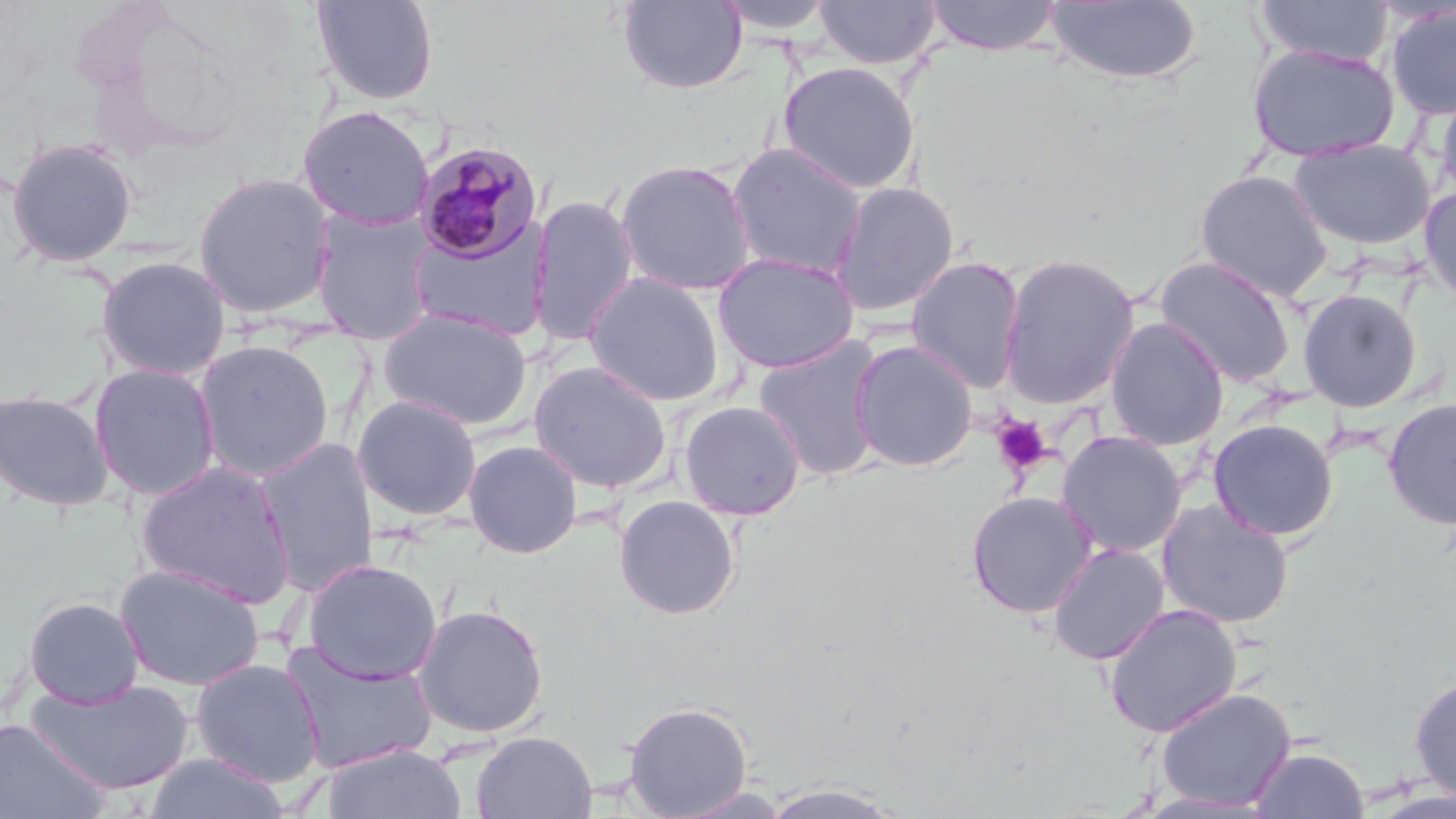
Approximate bounding boxes as named x1/y1/x2/y2 corners in pixels. Uninfected red blood cell locations: (x1=311, y1=0, x2=440, y2=105), (x1=712, y1=0, x2=839, y2=35), (x1=923, y1=0, x2=1065, y2=56), (x1=1253, y1=0, x2=1395, y2=67), (x1=617, y1=1, x2=747, y2=94), (x1=813, y1=1, x2=942, y2=69), (x1=1043, y1=1, x2=1202, y2=84), (x1=1385, y1=5, x2=1456, y2=120), (x1=1246, y1=43, x2=1400, y2=164), (x1=778, y1=61, x2=920, y2=194), (x1=1435, y1=81, x2=1456, y2=205), (x1=297, y1=105, x2=436, y2=230), (x1=4, y1=136, x2=139, y2=268), (x1=1289, y1=138, x2=1436, y2=251), (x1=726, y1=142, x2=868, y2=280), (x1=615, y1=159, x2=758, y2=296), (x1=1194, y1=169, x2=1334, y2=301), (x1=192, y1=171, x2=337, y2=319), (x1=829, y1=180, x2=960, y2=317), (x1=1419, y1=185, x2=1456, y2=305), (x1=528, y1=195, x2=639, y2=347), (x1=308, y1=207, x2=438, y2=344), (x1=404, y1=224, x2=552, y2=343), (x1=712, y1=251, x2=860, y2=374), (x1=997, y1=253, x2=1141, y2=410), (x1=95, y1=255, x2=232, y2=381), (x1=905, y1=255, x2=1026, y2=393), (x1=1155, y1=255, x2=1298, y2=388), (x1=582, y1=272, x2=727, y2=407), (x1=1296, y1=288, x2=1424, y2=413), (x1=378, y1=307, x2=533, y2=429), (x1=1105, y1=317, x2=1229, y2=451), (x1=751, y1=335, x2=887, y2=481), (x1=194, y1=339, x2=334, y2=481), (x1=849, y1=340, x2=979, y2=472), (x1=528, y1=360, x2=673, y2=493), (x1=88, y1=362, x2=222, y2=500), (x1=0, y1=388, x2=115, y2=511), (x1=352, y1=394, x2=483, y2=522), (x1=1383, y1=397, x2=1456, y2=530), (x1=678, y1=399, x2=806, y2=520), (x1=1207, y1=418, x2=1339, y2=541), (x1=1056, y1=430, x2=1188, y2=557), (x1=254, y1=439, x2=380, y2=595), (x1=463, y1=439, x2=583, y2=558), (x1=136, y1=459, x2=296, y2=607), (x1=966, y1=490, x2=1098, y2=618), (x1=613, y1=495, x2=741, y2=620), (x1=1155, y1=499, x2=1295, y2=629), (x1=1046, y1=541, x2=1170, y2=665), (x1=301, y1=558, x2=443, y2=685), (x1=113, y1=563, x2=266, y2=691), (x1=23, y1=596, x2=146, y2=708), (x1=411, y1=603, x2=549, y2=740), (x1=1103, y1=603, x2=1242, y2=738), (x1=280, y1=642, x2=437, y2=775), (x1=189, y1=657, x2=326, y2=787), (x1=1409, y1=671, x2=1456, y2=803), (x1=24, y1=677, x2=192, y2=798), (x1=1154, y1=687, x2=1297, y2=812), (x1=623, y1=700, x2=753, y2=818), (x1=0, y1=716, x2=111, y2=818), (x1=470, y1=730, x2=597, y2=819), (x1=320, y1=742, x2=468, y2=819), (x1=1249, y1=745, x2=1369, y2=818), (x1=143, y1=751, x2=291, y2=819), (x1=757, y1=781, x2=911, y2=819). Plasmodium malariae-infected red blood cell locations: (x1=412, y1=140, x2=545, y2=265). Platelet locations: (x1=990, y1=415, x2=1052, y2=477). Slide-level diagnosis: Plasmodium malariae. Captured at 1000x magnification. One field of a larger specimen. Thin blood smear. Light microscopy. May-Grünwald-Giemsa-stained preparation. Image is 1456×819 pixels.